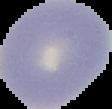

image_size: 112×109 pixels
image_type: cell region segmented out of the field of view; surrounding area masked to black
preparation: thin blood film
result: no malaria parasites detected